State which cell type is depicted.
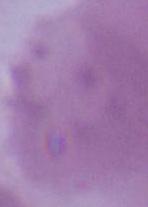
This is an erythrocyte.

magnification = 1000x
modality = micrograph